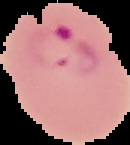

{
  "preparation": "thin blood smear",
  "image_size": "130×145 pixels",
  "malaria_status": "parasitized",
  "image_type": "segmented cell region with the area outside set to black"
}